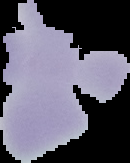 From a thin blood smear. Image is 130×163 pixels. Result: no Plasmodium parasites seen. Cell region segmented out of the field of view; the surrounding area is masked to black.